Classify this cell by malaria status.
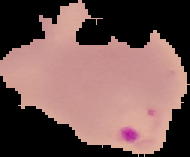
It is parasitized.

Summary:
  - Image type: segmented cell region with the area outside set to black
  - Image size: 190×157 pixels
  - Preparation: thin blood film